Classify this cell by malaria status.
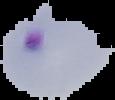
It is parasitized.

Image is 115×100 pixels. From a thin blood film. Segmented cell region on a black background.